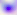

magnification = 400x
identification = Toxoplasma gondii
modality = photomicrograph